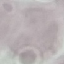

{
  "malaria_status": "uninfected",
  "capture": "smartphone camera at the microscope eyepiece",
  "image_type": "cell patch, automatically extracted from a larger field of view and resized to 64 × 64 pixels",
  "stain": "Giemsa",
  "preparation": "thin blood smear"
}